Report the malaria status of this cell.
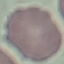

It is uninfected.

capture = smartphone through the microscope eyepiece
stain = Giemsa
image type = automatically extracted cell patch, resized to 64 × 64 pixels
preparation = thin smear